Assess the morphology of the red blood cells.
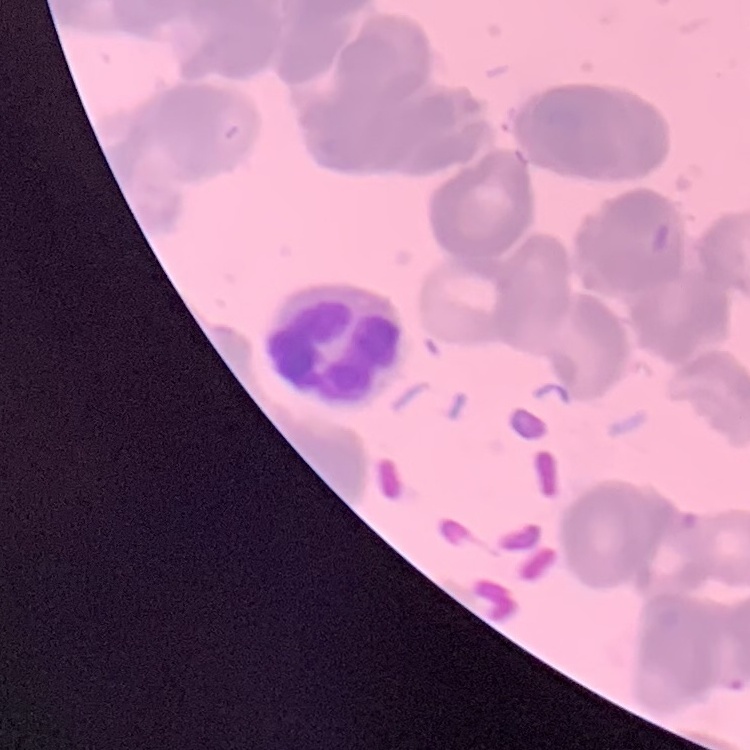

They show rouleaux formation.

One tile cut from a larger photomicrograph. Stained with either Field's or Giemsa. Thin blood smear.